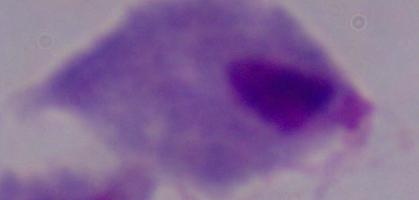

modality: photomicrograph
identification: trichomonad
magnification: 1000x